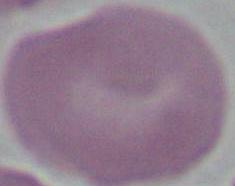

Summary:
  - Magnification: 1000x
  - Modality: photomicrograph
  - Identification: red blood cell